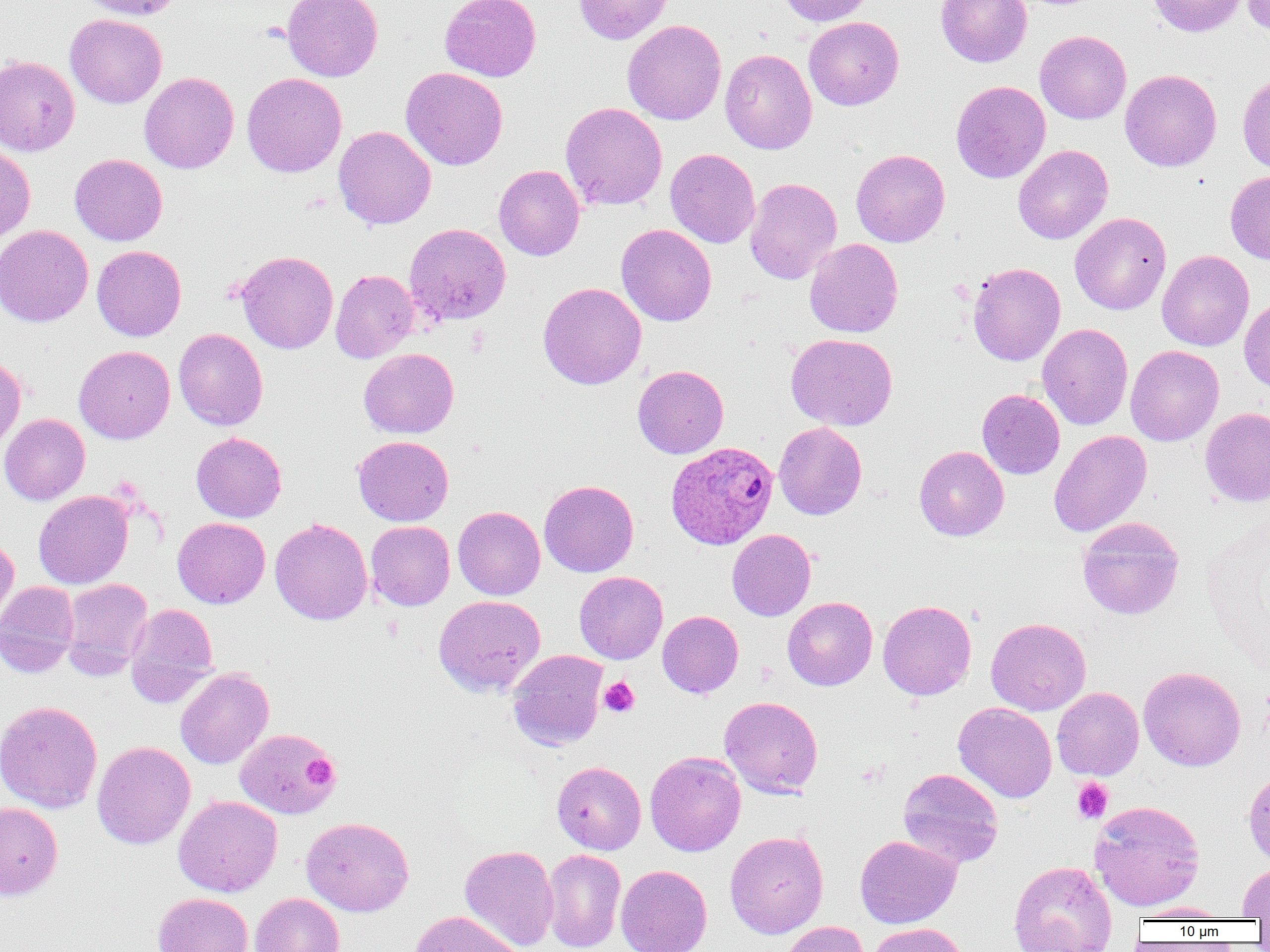
slide-level diagnosis = Plasmodium ovale
platelet locations = approximate bounding boxes as (x1, y1, x2, y2) in pixels: (598, 677, 639, 717), (303, 754, 339, 789), (1073, 778, 1113, 823)
uninfected red blood cell locations = approximate bounding boxes as (x1, y1, x2, y2) in pixels: (77, 0, 183, 20), (281, 0, 383, 81), (440, 0, 540, 82), (573, 0, 674, 44), (777, 0, 874, 26), (936, 0, 1032, 67), (1147, 0, 1249, 37), (1242, 0, 1270, 35), (65, 14, 167, 108), (804, 16, 904, 110), (622, 20, 727, 125), (1035, 30, 1131, 124), (719, 48, 817, 154), (0, 55, 80, 156), (400, 67, 508, 170), (1120, 69, 1222, 171), (139, 72, 239, 173), (241, 72, 347, 177), (1237, 72, 1270, 175), (951, 80, 1051, 183), (560, 102, 667, 210), (333, 126, 436, 230), (0, 142, 35, 243), (1013, 144, 1113, 244), (665, 148, 760, 248), (851, 149, 950, 247), (70, 154, 168, 245), (494, 165, 585, 261), (1225, 171, 1270, 265), (744, 178, 842, 284), (1070, 212, 1171, 314), (404, 223, 511, 326), (0, 224, 93, 327), (615, 224, 716, 326), (804, 238, 903, 338), (92, 245, 186, 341), (236, 250, 338, 354), (1157, 250, 1254, 351), (967, 262, 1065, 366), (330, 269, 420, 363), (538, 282, 646, 389), (1239, 295, 1270, 392), (1037, 323, 1133, 430), (173, 328, 268, 430), (786, 333, 897, 430), (74, 345, 175, 444), (1125, 345, 1224, 446), (359, 348, 459, 438), (0, 355, 26, 453), (632, 365, 729, 459), (977, 389, 1065, 479), (1200, 407, 1270, 506), (0, 413, 90, 505), (774, 422, 867, 520), (1049, 430, 1152, 537), (191, 432, 287, 522), (353, 435, 454, 526), (914, 445, 1009, 541), (539, 479, 639, 577), (33, 490, 133, 589), (453, 506, 545, 600), (1077, 516, 1184, 620), (172, 517, 270, 609), (270, 518, 373, 625), (366, 521, 455, 610), (727, 529, 816, 621), (0, 535, 19, 631), (574, 571, 668, 664), (60, 578, 153, 680), (0, 581, 80, 678), (433, 595, 545, 697), (782, 597, 878, 691), (878, 600, 976, 700), (124, 603, 218, 707), (657, 610, 743, 698), (986, 617, 1091, 715), (508, 649, 608, 751), (1138, 666, 1246, 771), (175, 667, 274, 769), (1052, 687, 1144, 780), (719, 696, 823, 798), (0, 700, 103, 814), (953, 702, 1057, 803), (235, 727, 340, 819), (92, 741, 196, 849), (645, 751, 746, 856), (551, 761, 646, 854), (898, 768, 1003, 868), (1243, 770, 1270, 866), (173, 795, 282, 897), (1089, 800, 1205, 911), (0, 802, 63, 900), (301, 816, 414, 916), (725, 830, 828, 938), (855, 835, 961, 928), (459, 844, 559, 951), (541, 848, 626, 952), (1008, 860, 1117, 952), (1237, 861, 1270, 920), (615, 864, 712, 952), (153, 892, 253, 952), (250, 893, 344, 952), (1129, 903, 1231, 921), (409, 910, 524, 952), (780, 921, 869, 952), (868, 922, 969, 952)
Plasmodium ovale-infected red blood cell locations = approximate bounding boxes as (x1, y1, x2, y2) in pixels: (662, 445, 775, 555)
modality = optical microscopy
preparation = thin blood film
magnification = 1000x
image size = 1270×952 pixels
field of view = one of a larger specimen